Locate every malaria parasite.
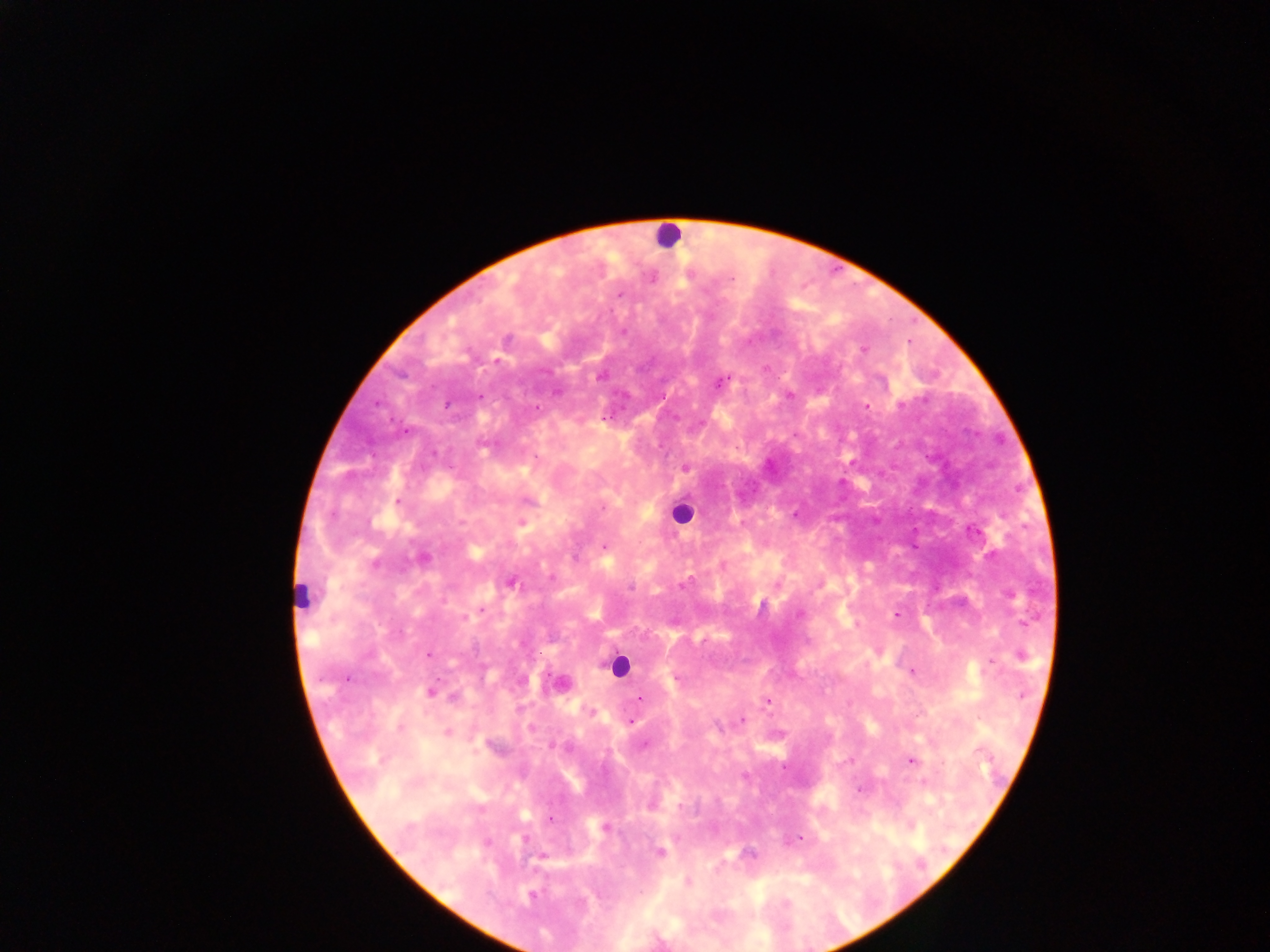

Approximate centers as [x, y] in pixels.
Malaria parasites: [731, 278], [620, 295], [622, 332], [507, 339], [863, 350], [600, 377], [721, 382], [790, 396], [479, 397], [446, 405], [901, 405], [536, 407], [866, 407], [606, 419], [407, 430], [535, 457], [685, 468], [398, 501], [528, 501], [603, 509], [521, 523], [971, 532], [604, 547], [424, 558], [375, 562], [511, 582], [683, 584], [630, 587], [482, 610], [799, 614], [896, 615], [464, 618], [428, 655], [1022, 655], [991, 661], [911, 672], [347, 678], [677, 680], [431, 693], [1022, 694], [453, 698], [639, 698], [767, 700], [591, 712], [741, 720], [631, 722], [718, 727], [400, 729], [447, 733], [552, 745], [645, 745], [850, 760], [911, 760], [861, 790], [550, 819], [605, 828], [799, 838], [487, 842], [660, 852], [688, 881], [532, 895].

Leukocyte locations: [668, 236], [681, 513], [299, 588], [618, 664]. Sample from Ghana. Image is 1270×952 pixels. Single field of view. Mobile-phone photograph taken through the microscope. Thick blood smear.